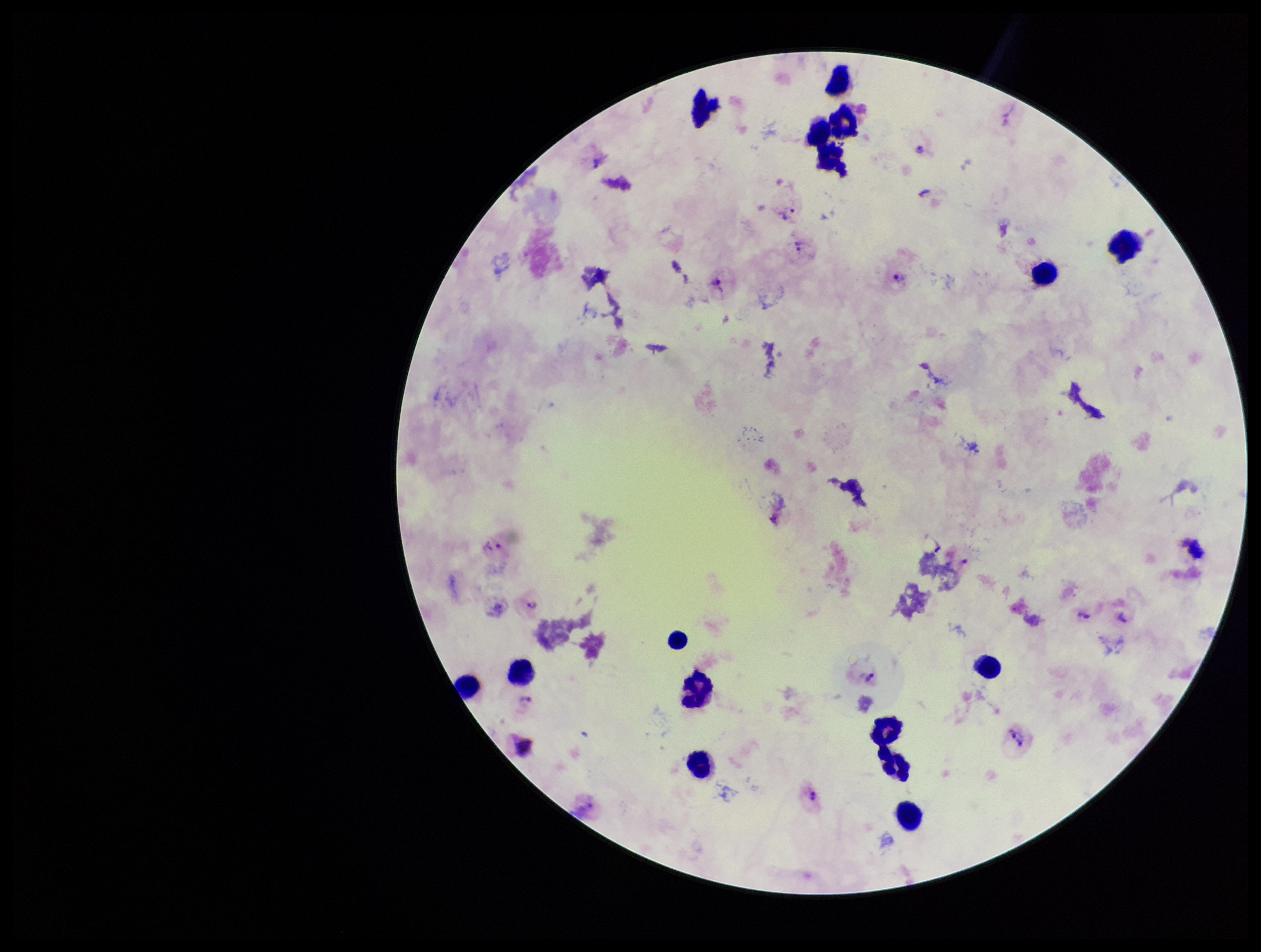
{
  "patient_malaria_status": "infected",
  "image_size": "1261×952 pixels",
  "plasmodium_parasites": "seen",
  "leukocyte_count": 16,
  "field_of_view": "single",
  "stain": "Giemsa",
  "parasite_count": 15,
  "species_reported_for_this_patient": "Plasmodium vivax",
  "preparation": "thick",
  "capture": "smartphone photograph through the microscope eyepiece"
}